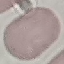

Summary:
  - Malaria status: uninfected
  - Capture: smartphone camera at the microscope eyepiece
  - Stain: Giemsa
  - Preparation: thin blood film
  - Image type: cell patch, automatically extracted from a larger field of view and resized to 64 × 64 pixels